Locate every Plasmodium parasite.
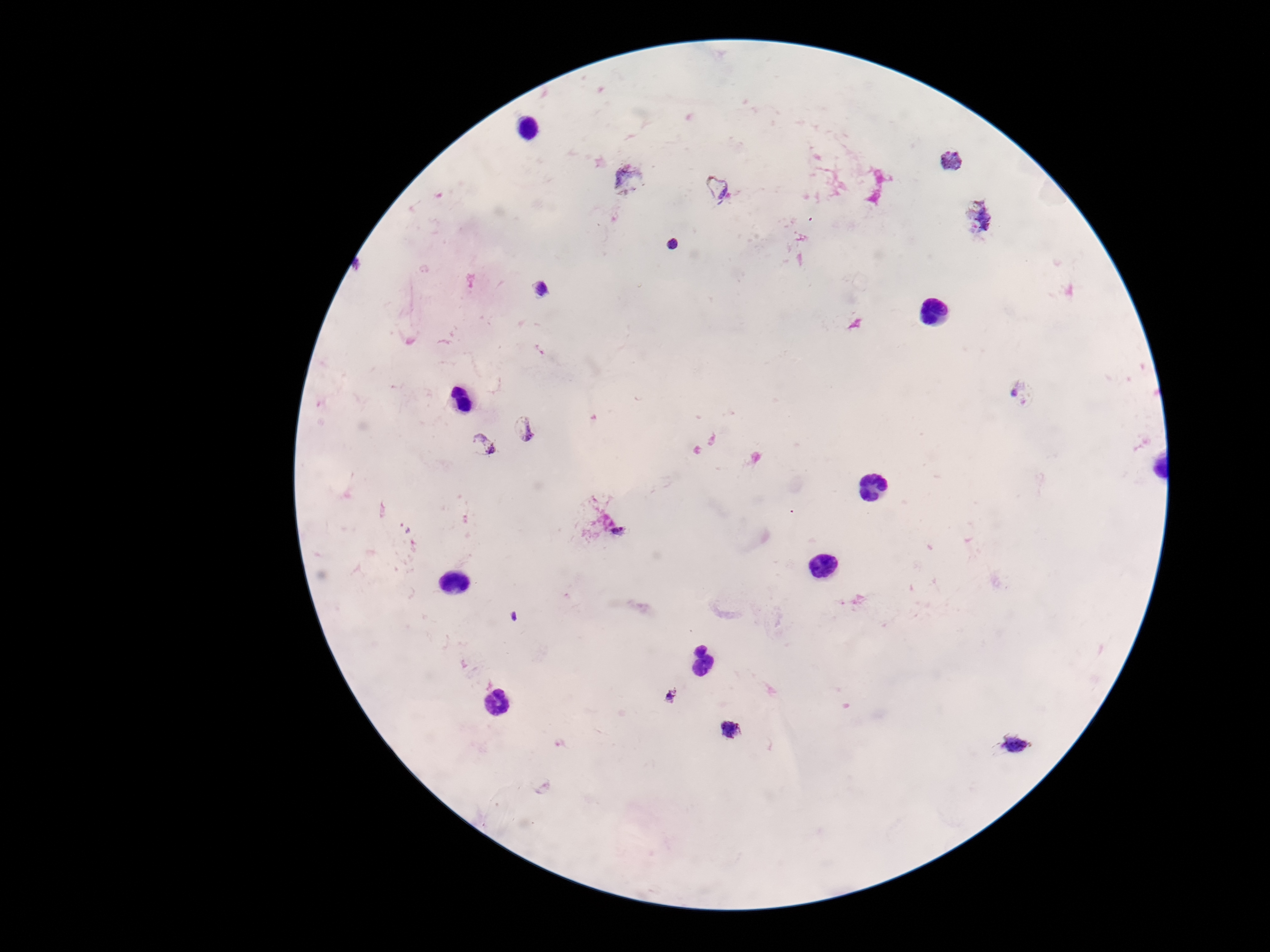

Approximate centers as {x, y} in pixels.
Plasmodium parasites: {951, 162}, {629, 177}, {718, 187}, {980, 218}, {672, 244}, {540, 289}, {1020, 393}, {526, 428}, {480, 445}, {615, 529}, {515, 617}, {672, 696}, {733, 729}, {1014, 744}.

patient malaria status = infected
stain = Giemsa
preparation = thick blood smear
capture = smartphone camera through the microscope eyepiece
image size = 1270×952 pixels
field of view = single
magnification = 100x